Describe the morphology of the red blood cells.
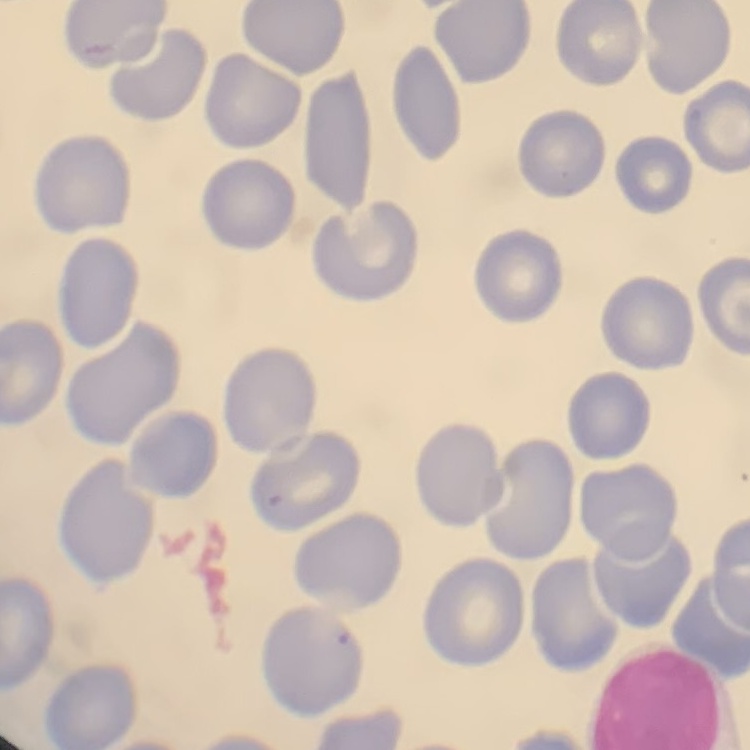

No rouleaux formation.

preparation: thin blood smear
image_type: square crop of a larger photomicrograph
stain: Field's or Giemsa